Locate every Plasmodium parasite.
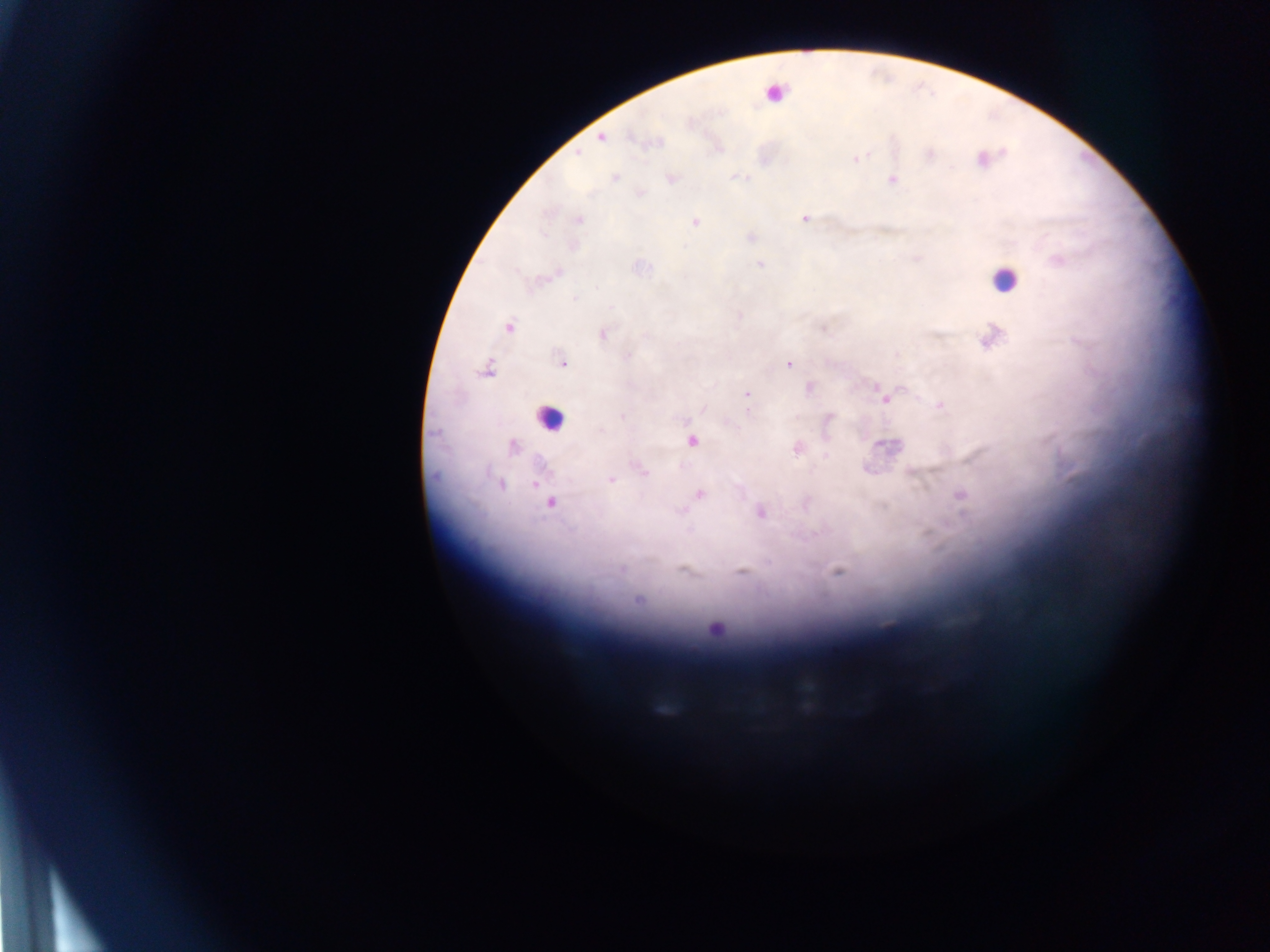

Approximate centers as x y in pixels.
Plasmodium parasites: 602 137; 578 152; 930 153; 856 159; 616 178; 892 180; 805 218; 578 219; 696 222; 1058 261; 760 264; 555 274; 574 299; 508 326; 824 329; 603 335; 991 339; 627 355; 562 363; 788 365; 487 370; 747 394; 882 395; 940 405; 622 416; 601 430; 692 440; 886 446; 512 447; 973 458; 643 470; 610 479; 535 483; 501 485; 699 494; 960 495; 551 503; 760 513; 622 570; 837 571; 741 572; 638 601; 714 628.

Leukocyte locations: 777 91; 1003 280; 550 417. Collected in Ghana. Thick blood film. Photographed through a microscope with a mobile-phone camera. One field of view. Image is 1270×952 pixels.